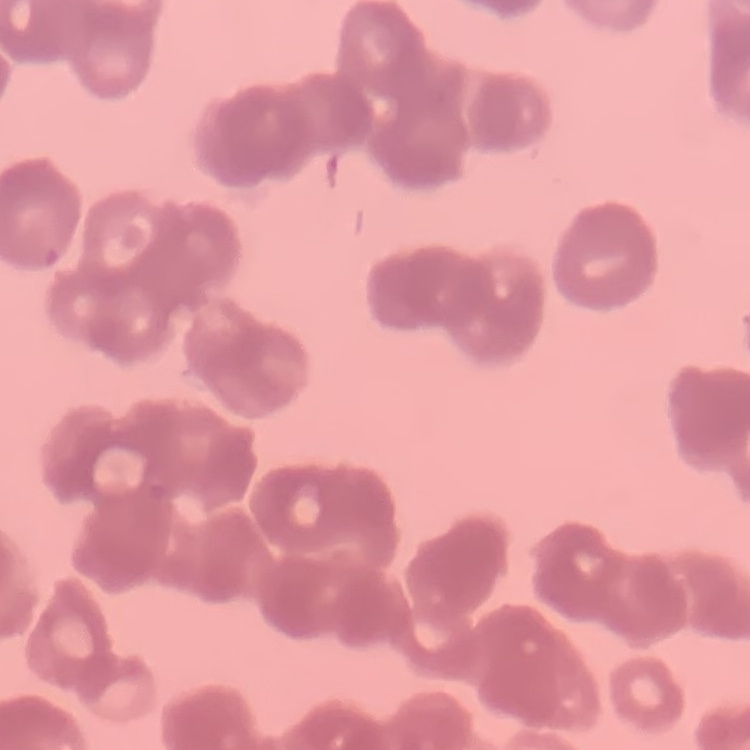
{
  "erythrocyte_morphology": "rouleaux formation",
  "image_type": "one tile cut from a larger photomicrograph",
  "preparation": "thin blood film",
  "stain": "Field's or Giemsa"
}